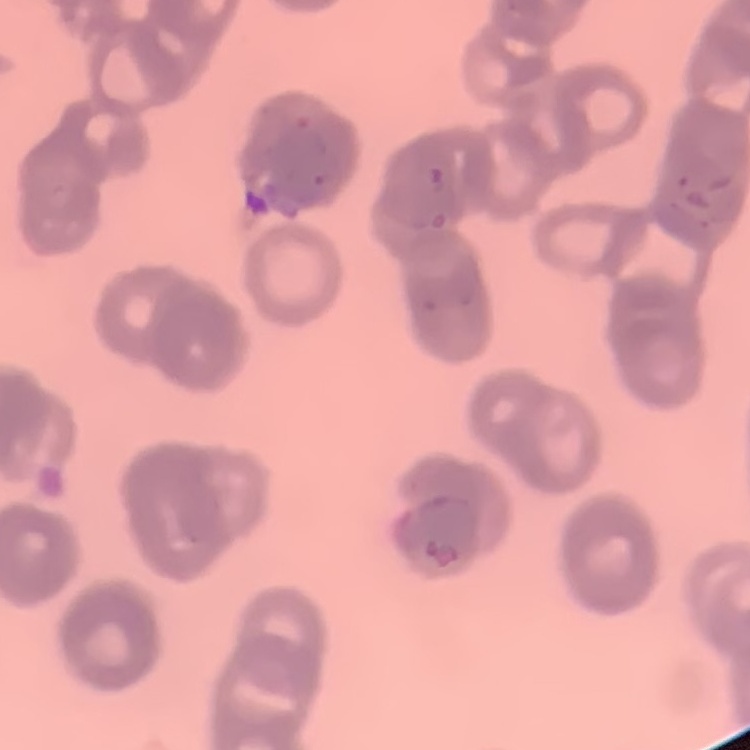

Summary:
  - Erythrocyte morphology: rouleaux formation
  - Stain: Field's or Giemsa
  - Image type: square crop of a larger photomicrograph
  - Preparation: thin blood film